Classify this cell by malaria status.
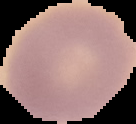
It is uninfected.

preparation = thin blood smear
image type = segmented cell region on a black background
image size = 136×124 pixels